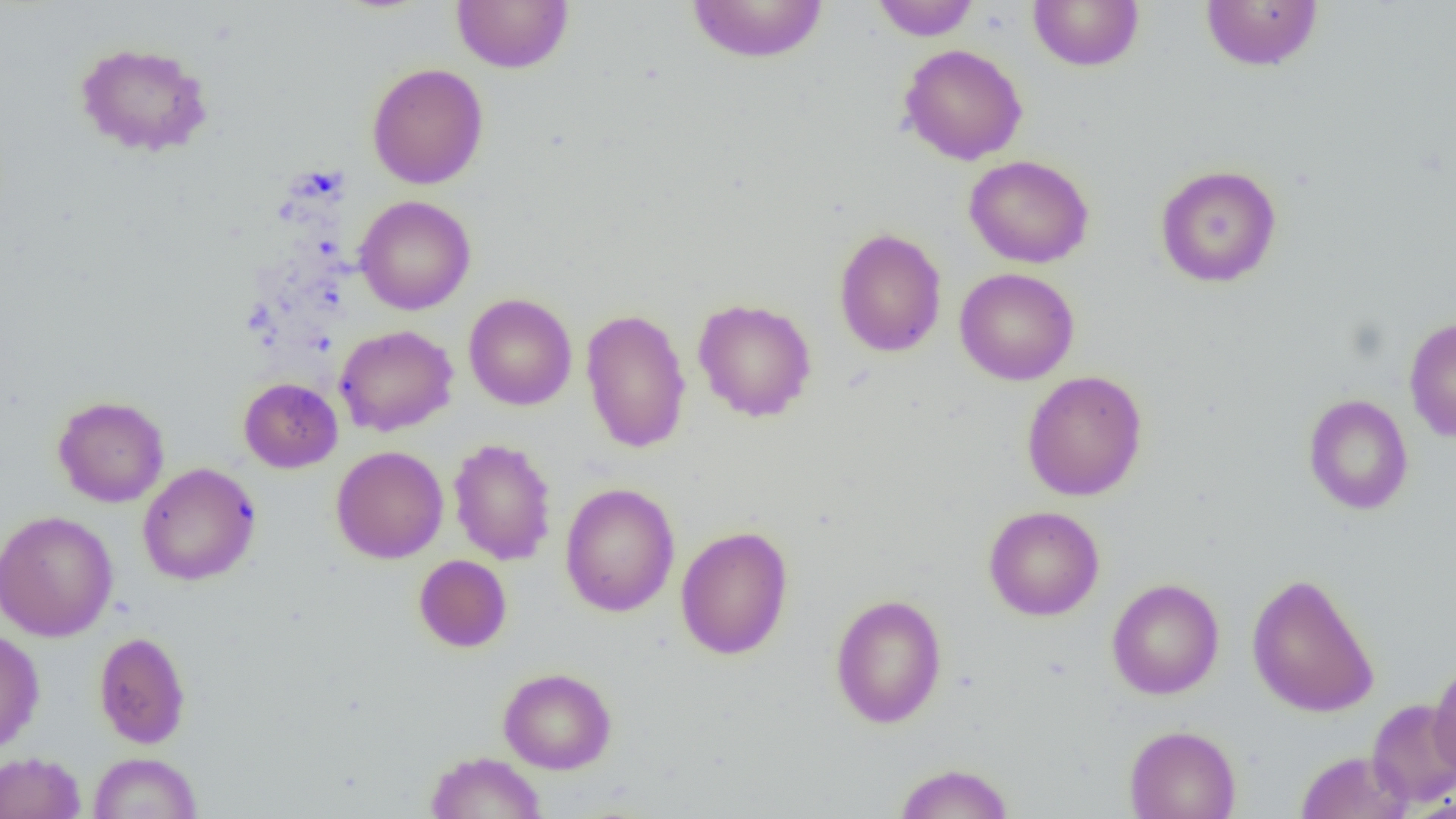
Approximate bounding boxes as named x1/y1/x2/y2 corners in pixels. Uninfected red blood cell locations: (x1=451, y1=0, x2=574, y2=73), (x1=686, y1=0, x2=829, y2=64), (x1=870, y1=0, x2=981, y2=41), (x1=1029, y1=0, x2=1144, y2=71), (x1=1200, y1=0, x2=1323, y2=71), (x1=74, y1=41, x2=214, y2=158), (x1=899, y1=43, x2=1028, y2=165), (x1=366, y1=63, x2=489, y2=189), (x1=964, y1=155, x2=1094, y2=268), (x1=1155, y1=164, x2=1282, y2=288), (x1=354, y1=195, x2=476, y2=315), (x1=833, y1=227, x2=947, y2=358), (x1=954, y1=267, x2=1079, y2=386), (x1=463, y1=293, x2=577, y2=410), (x1=693, y1=297, x2=817, y2=422), (x1=580, y1=307, x2=692, y2=454), (x1=1404, y1=316, x2=1456, y2=442), (x1=335, y1=324, x2=458, y2=437), (x1=1021, y1=370, x2=1148, y2=501), (x1=239, y1=378, x2=342, y2=473), (x1=1303, y1=393, x2=1414, y2=515), (x1=52, y1=395, x2=169, y2=507), (x1=447, y1=438, x2=557, y2=566), (x1=331, y1=445, x2=448, y2=564), (x1=137, y1=462, x2=261, y2=586), (x1=559, y1=483, x2=680, y2=616), (x1=984, y1=505, x2=1104, y2=621), (x1=0, y1=510, x2=118, y2=642), (x1=675, y1=525, x2=794, y2=660), (x1=414, y1=554, x2=512, y2=652), (x1=1246, y1=571, x2=1380, y2=718), (x1=1106, y1=578, x2=1224, y2=700), (x1=830, y1=593, x2=947, y2=729), (x1=0, y1=628, x2=45, y2=754), (x1=93, y1=631, x2=191, y2=749), (x1=1429, y1=661, x2=1456, y2=779), (x1=498, y1=667, x2=617, y2=774), (x1=1367, y1=699, x2=1456, y2=808), (x1=1124, y1=725, x2=1241, y2=819), (x1=1295, y1=750, x2=1412, y2=819), (x1=0, y1=751, x2=86, y2=819), (x1=426, y1=751, x2=546, y2=819), (x1=88, y1=752, x2=202, y2=819), (x1=892, y1=762, x2=1015, y2=819). Slide-level diagnosis: no evidence of blood parasites. Optical microscopy. Captured at 1000x magnification. One field of a larger specimen. Image is 1456×819 pixels. Thin blood film.